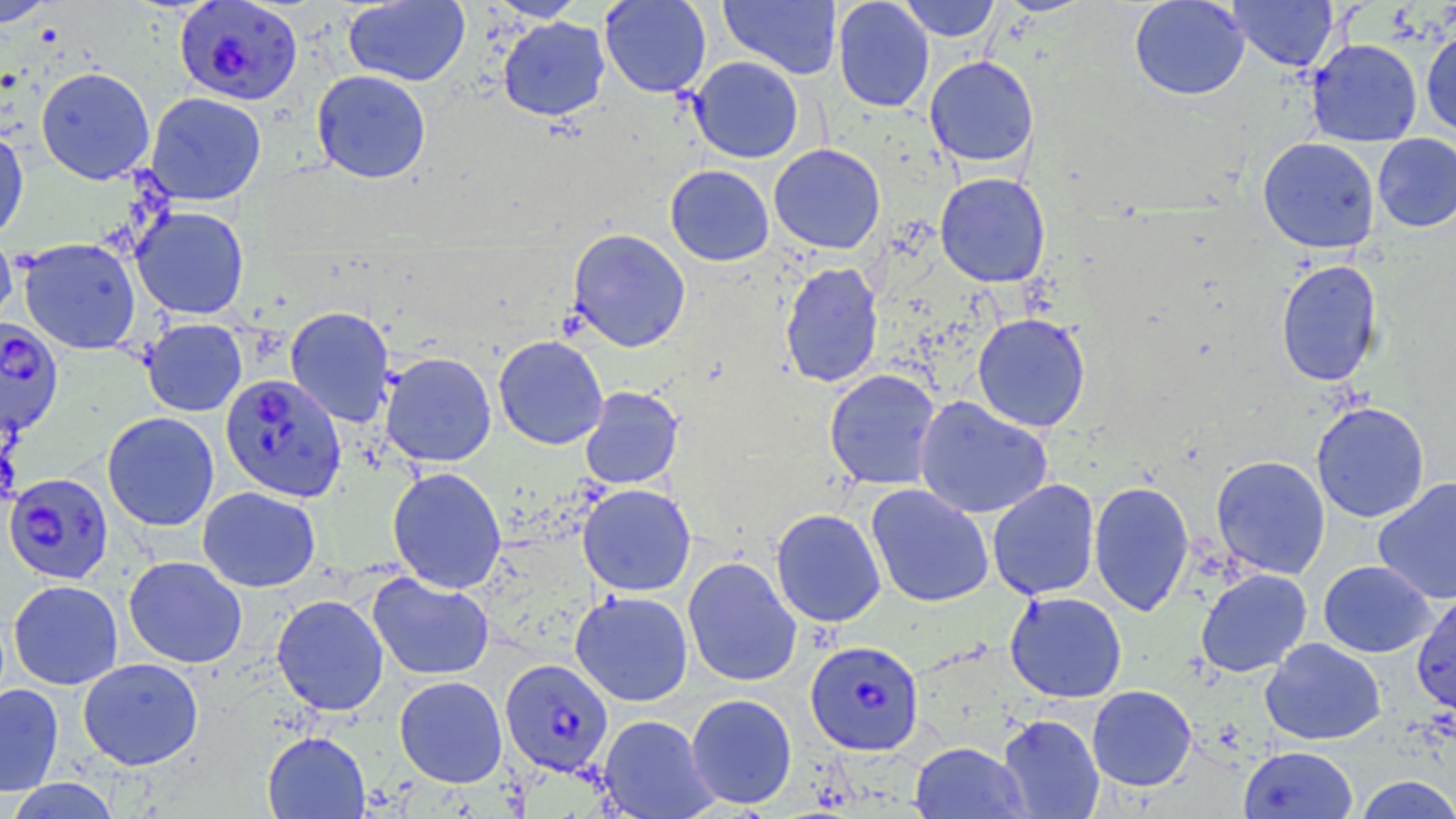 Approximate bounding boxes as [x1, y1, x2, y2] in pixels. Uninfected red blood cell locations: [0, 0, 59, 27], [486, 0, 587, 21], [599, 0, 712, 98], [718, 0, 842, 80], [833, 0, 934, 112], [898, 0, 1001, 42], [993, 0, 1096, 17], [1129, 0, 1250, 100], [1228, 0, 1338, 71], [343, 1, 470, 87], [498, 17, 610, 121], [1420, 30, 1456, 137], [1306, 38, 1422, 147], [924, 55, 1039, 168], [688, 56, 804, 163], [36, 67, 155, 184], [311, 72, 431, 186], [145, 92, 267, 206], [0, 126, 29, 241], [1372, 133, 1456, 232], [1258, 137, 1380, 253], [768, 144, 885, 254], [665, 165, 775, 266], [935, 172, 1051, 287], [131, 206, 250, 320], [0, 227, 17, 334], [566, 228, 691, 352], [18, 238, 141, 355], [1275, 259, 1383, 387], [779, 262, 884, 388], [285, 306, 395, 428], [972, 313, 1091, 432], [140, 318, 247, 416], [493, 335, 609, 450], [380, 351, 497, 467], [824, 369, 941, 491], [579, 386, 684, 490], [914, 396, 1053, 519], [1311, 402, 1430, 523], [102, 412, 220, 531], [1211, 455, 1330, 579], [387, 467, 507, 594], [1373, 477, 1456, 605], [987, 479, 1100, 601], [1088, 480, 1194, 616], [577, 483, 696, 596], [865, 484, 994, 608], [197, 486, 321, 592], [770, 508, 886, 628], [123, 556, 248, 668], [682, 556, 802, 687], [1318, 560, 1436, 658], [1196, 568, 1312, 677], [367, 572, 495, 681], [8, 580, 123, 690], [1411, 589, 1456, 716], [570, 590, 693, 706], [1004, 591, 1127, 703], [271, 594, 389, 716], [1260, 638, 1386, 745], [78, 657, 204, 770], [394, 676, 508, 788], [0, 683, 64, 796], [1087, 685, 1196, 791], [685, 693, 797, 810], [997, 714, 1105, 818], [598, 715, 718, 818], [262, 730, 371, 818], [909, 742, 1030, 818], [1238, 746, 1359, 819], [1354, 775, 1456, 818], [6, 778, 122, 818]. Plasmodium falciparum-infected red blood cell locations: [174, 0, 303, 106], [0, 314, 68, 440], [220, 373, 347, 502], [4, 473, 114, 584], [805, 639, 924, 755], [499, 658, 616, 780]. Slide-level diagnosis: Plasmodium falciparum. May-Grünwald-Giemsa stain. One field of a larger specimen. 1000x magnification. Image is 1456×819 pixels. Optical microscopy. Thin blood smear.